Mark where leukocytes are.
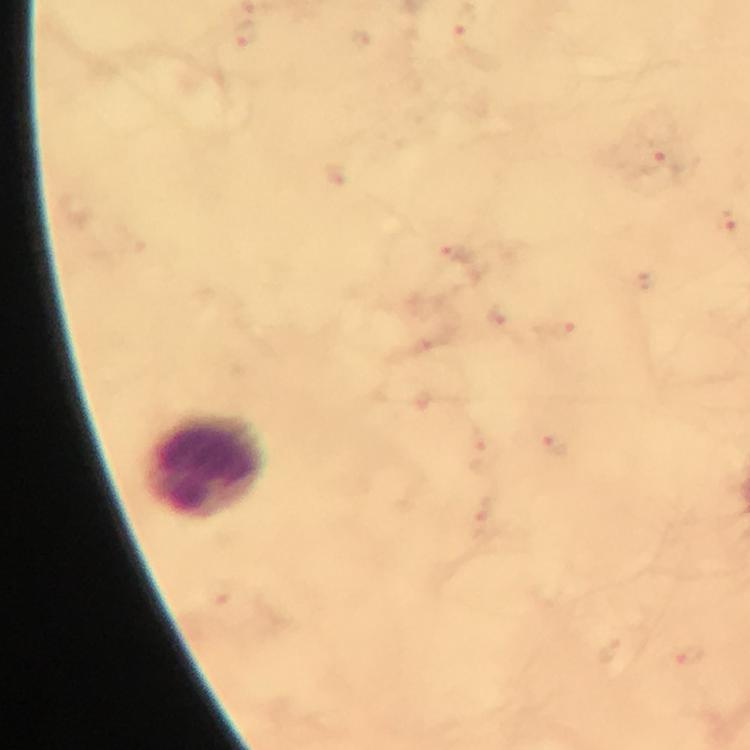
Approximate object centers, in pixels from the top-left corner.
Leukocytes: (x=207, y=467).

stain = Giemsa
capture = smartphone camera through the microscope
malaria parasites = none seen
magnification = 100x
image size = 750×750 pixels
cropped from = one field of view
context = from a diagnostic examination for malaria
preparation = thick blood film
immersion oil = used